State which cell type is depicted.
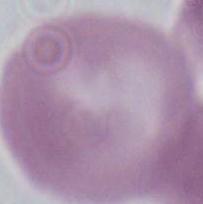
This is an erythrocyte.

Captured at 1000x magnification. Micrograph.